State the blood parasite species.
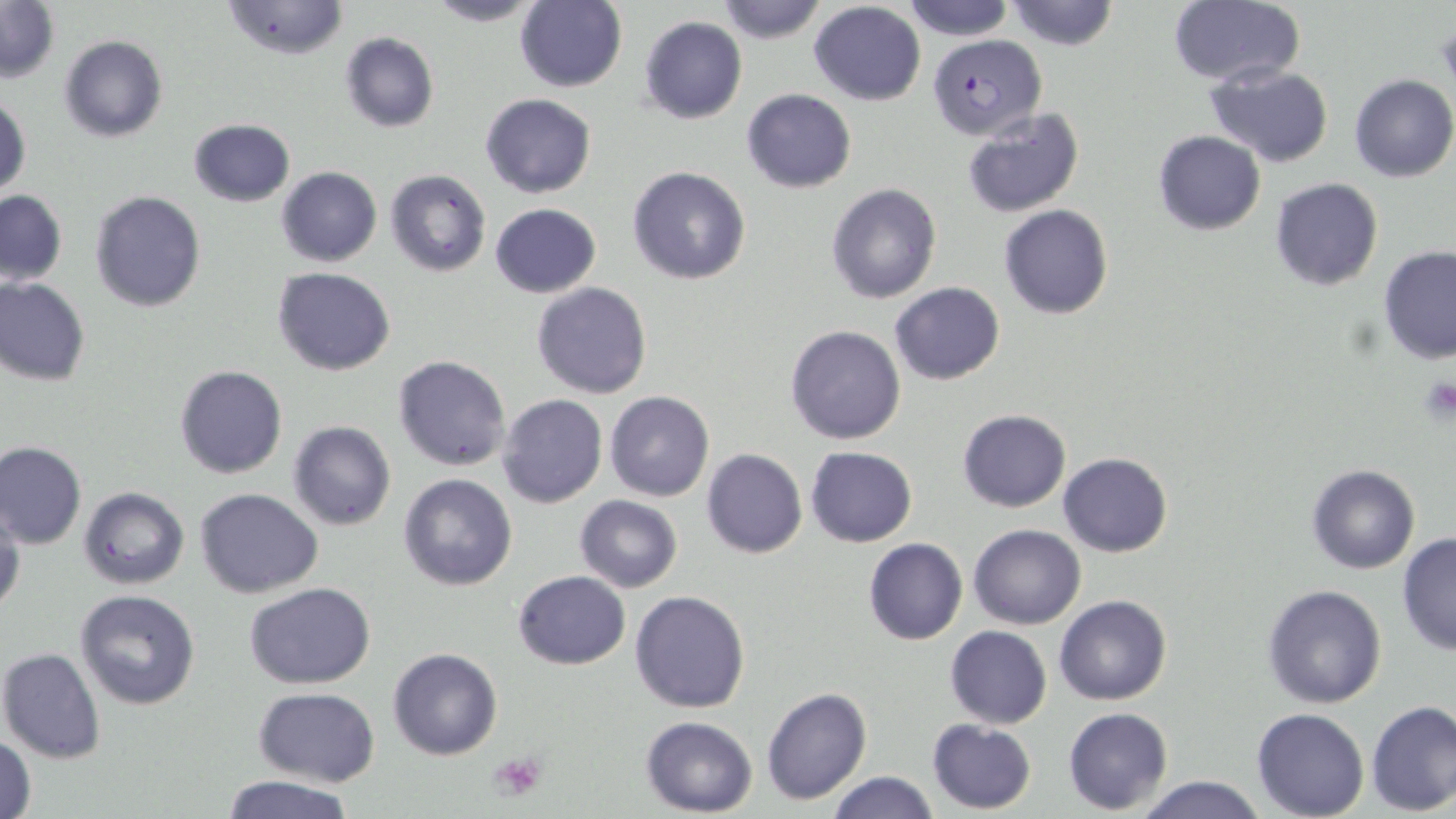

Plasmodium falciparum.

Summary:
  - Coordinate format: approximate bounding boxes as [x1, y1, x2, y2] in pixels
  - Uninfected red blood cell locations: [0, 0, 58, 83], [419, 0, 548, 27], [714, 0, 828, 44], [900, 0, 1015, 41], [1005, 0, 1121, 52], [1167, 0, 1304, 88], [219, 1, 350, 60], [514, 1, 627, 92], [809, 2, 927, 106], [640, 16, 747, 123], [339, 32, 440, 133], [59, 34, 167, 142], [1205, 66, 1334, 165], [1349, 75, 1455, 183], [740, 88, 856, 193], [1, 89, 31, 199], [481, 93, 596, 199], [959, 107, 1086, 219], [187, 118, 295, 207], [1153, 130, 1267, 235], [626, 165, 752, 285], [277, 167, 382, 266], [386, 169, 492, 277], [1269, 178, 1384, 291], [825, 182, 941, 303], [0, 190, 68, 287], [91, 190, 206, 313], [489, 203, 601, 298], [997, 203, 1113, 321], [1378, 245, 1456, 365], [273, 268, 396, 376], [0, 276, 91, 386], [532, 282, 653, 400], [890, 282, 1005, 385], [785, 324, 907, 445], [393, 355, 511, 471], [174, 365, 288, 478], [605, 391, 714, 501], [498, 395, 607, 508], [957, 409, 1071, 512], [288, 421, 396, 531], [0, 441, 86, 549], [804, 446, 916, 547], [701, 448, 807, 559], [1058, 452, 1172, 558], [1306, 464, 1420, 573], [399, 474, 518, 591], [79, 487, 190, 590], [195, 487, 324, 598], [575, 495, 683, 592], [1, 501, 24, 620], [970, 525, 1085, 629], [1397, 532, 1456, 657], [864, 537, 967, 645], [513, 569, 631, 670], [246, 582, 376, 689], [1261, 584, 1387, 708], [630, 589, 750, 713], [75, 590, 202, 710], [1055, 595, 1173, 706], [945, 625, 1052, 730], [1, 648, 106, 764], [389, 648, 503, 761], [253, 687, 379, 785], [761, 687, 872, 804], [1366, 701, 1456, 815], [1064, 707, 1174, 814], [1251, 708, 1370, 819], [641, 715, 758, 815], [927, 720, 1036, 813], [1, 735, 37, 819], [827, 771, 941, 819], [218, 776, 360, 818], [1132, 776, 1271, 819]
  - Plasmodium falciparum-infected red blood cell locations: [928, 34, 1046, 139]
  - Platelet locations: [1417, 375, 1455, 423], [489, 751, 545, 802]
  - Modality: light microscopy
  - Image size: 1456×819 pixels
  - Stain: May-Grünwald-Giemsa
  - Magnification: 1000x
  - Field of view: single
  - Preparation: thin blood smear